Report the malaria status of this cell.
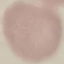

It is uninfected.

preparation = thin blood film
image type = cell patch, automatically extracted from a larger field of view and resized to 64 × 64 pixels
stain = Giemsa
capture = smartphone through the microscope eyepiece